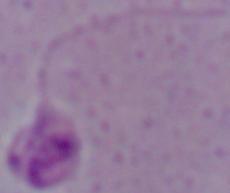
modality: micrograph
magnification: 1000x
identification: Leishmania